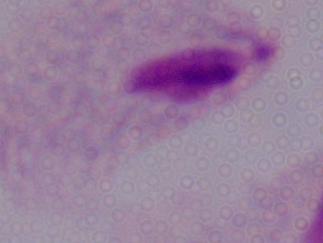
magnification = 1000x
modality = photomicrograph
identification = trichomonad